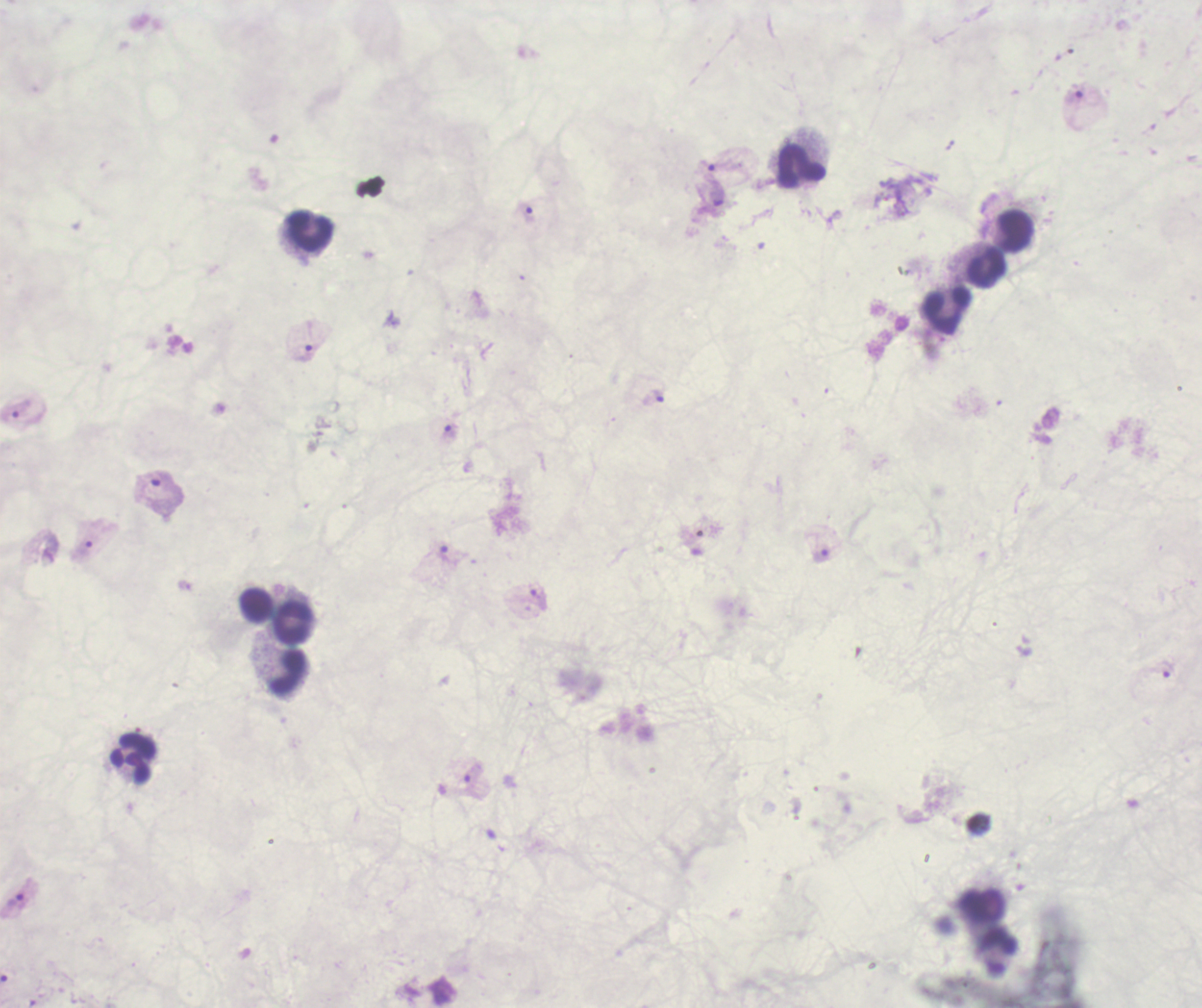

coordinate format = approximate centers as {x, y} in pixels
leukocyte locations = {800, 165}, {1014, 231}, {308, 233}, {984, 269}, {948, 311}, {256, 604}, {292, 624}, {289, 671}, {134, 759}
trophozoite locations = {715, 195}, {525, 212}, {306, 351}, {658, 398}, {446, 432}, {448, 555}, {821, 555}, {538, 600}, {1168, 669}, {17, 901}
magnification = 100x
image size = 1202×1008 pixels
context = previously used in a real diagnosis
result = positive for Plasmodium parasites
preparation = thick blood smear
stain = Romanowsky
field of view = one from this slide
background quality = poor